Outline each blood parasite and name the species.
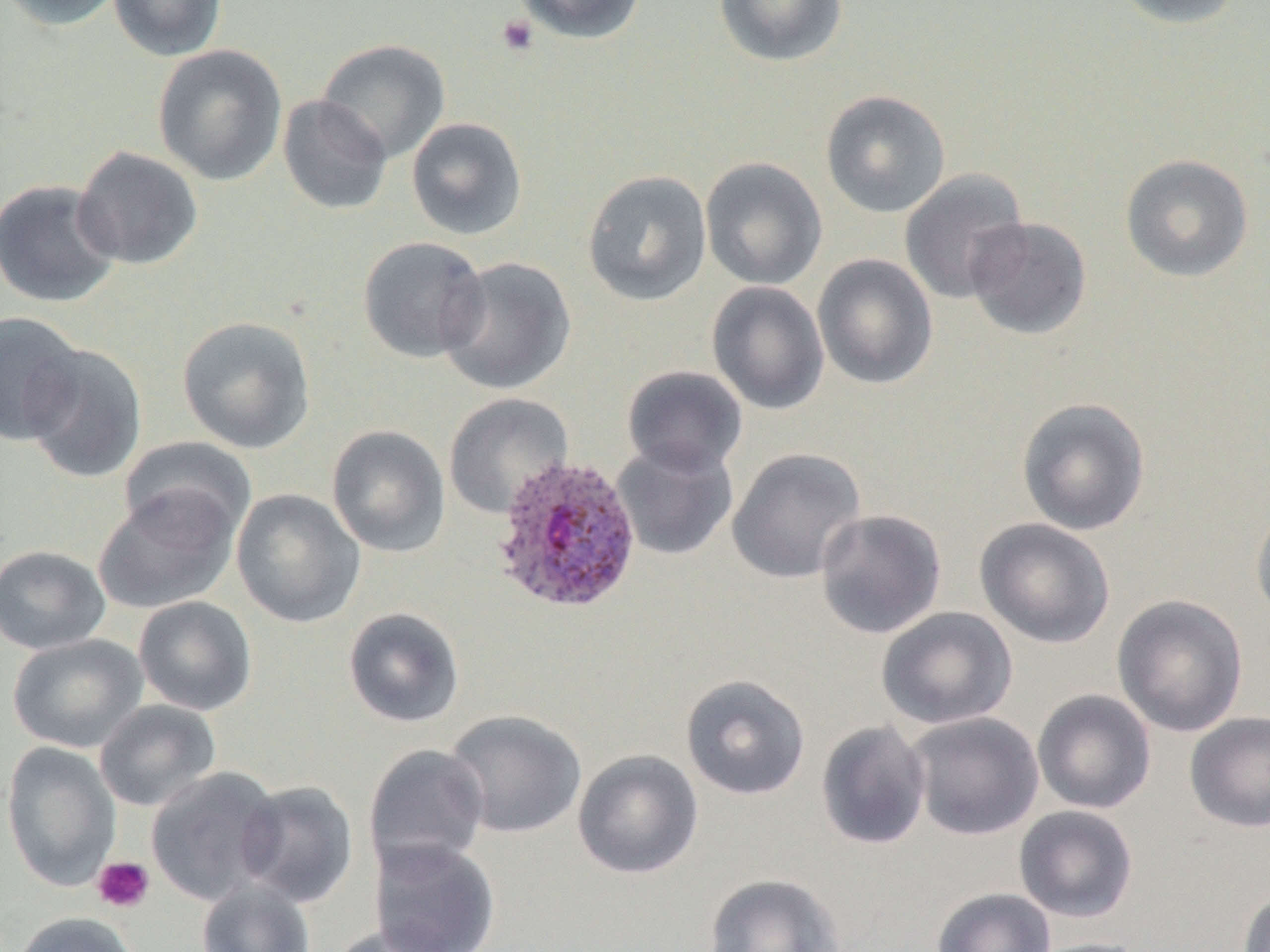
Approximate bounding boxes as (x1, y1, x2, y2) in pixels.
Plasmodium ovale-infected red blood cells: (491, 454, 642, 615).
No Plasmodium falciparum, Plasmodium malariae, Plasmodium vivax, Babesia divergens, or Trypanosoma brucei observed.

slide_level_diagnosis: Plasmodium ovale
preparation: thin blood film
field_of_view: one of a larger specimen
magnification: 1000x
platelet_locations: 'approximate bounding boxes as (x1, y1, x2, y2) in pixels: (495, 15, 540, 57), (92, 856, 155, 913)'
image_size: 1270×952 pixels
modality: light microscopy
uninfected_red_blood_cell_locations: 'approximate bounding boxes as (x1, y1, x2, y2) in pixels: (1, 0, 126, 31), (107, 0, 228, 62), (513, 0, 646, 45), (713, 0, 849, 67), (1109, 0, 1245, 29), (315, 38, 451, 163), (152, 44, 288, 186), (820, 89, 951, 218), (277, 95, 393, 216), (406, 116, 528, 240), (72, 146, 203, 271), (1120, 153, 1254, 283), (700, 157, 828, 290), (899, 168, 1030, 305), (582, 169, 713, 307), (0, 179, 121, 308), (965, 216, 1092, 340), (358, 236, 489, 364), (812, 253, 938, 390), (436, 255, 577, 395), (706, 281, 829, 415), (0, 310, 85, 447), (176, 315, 316, 454), (22, 343, 148, 484), (622, 365, 748, 475), (443, 393, 574, 519), (1016, 397, 1151, 536), (327, 425, 450, 558), (118, 437, 256, 546), (611, 439, 738, 560), (727, 448, 867, 584), (92, 487, 239, 615), (231, 488, 365, 628), (1251, 498, 1270, 627), (814, 508, 947, 639), (975, 517, 1116, 649), (0, 545, 111, 655), (1112, 594, 1248, 737), (133, 596, 257, 716), (342, 607, 465, 728), (876, 607, 1018, 730), (7, 634, 148, 753), (680, 673, 811, 801), (1032, 689, 1157, 815), (94, 699, 221, 812), (443, 709, 586, 839), (1185, 711, 1270, 833), (905, 712, 1044, 841), (816, 720, 931, 850), (1, 740, 122, 892), (363, 743, 490, 876), (572, 749, 704, 879), (145, 766, 284, 907), (236, 780, 359, 907), (1014, 805, 1138, 922), (368, 837, 501, 952), (703, 872, 845, 952), (197, 880, 316, 952), (931, 887, 1057, 952), (1237, 888, 1270, 952), (9, 911, 143, 952), (330, 922, 463, 952), (1023, 937, 1155, 952)'